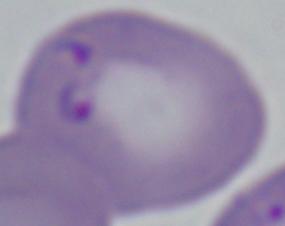

1000x magnification. A Babesia parasite is seen. Micrograph.